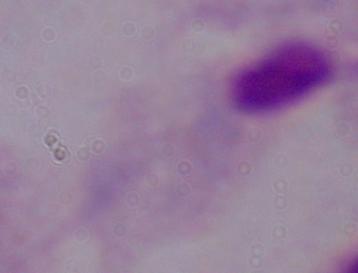

identification = trichomonad
magnification = 1000x
modality = photomicrograph